Give the position of every leukocyte visible.
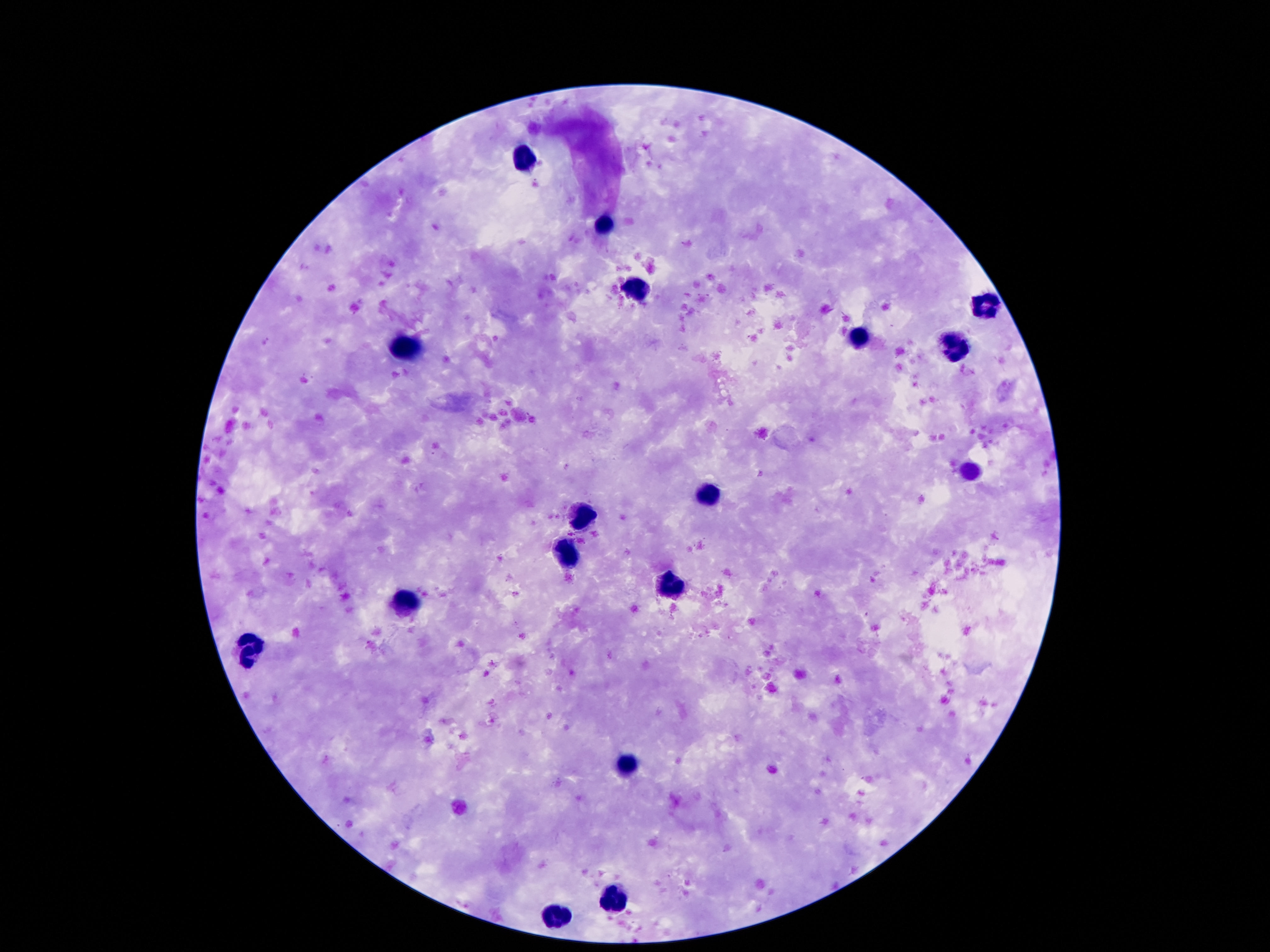
Approximate centers as {x, y} in pixels.
Leukocytes: {528, 160}, {604, 225}, {635, 286}, {984, 307}, {860, 339}, {954, 346}, {408, 347}, {711, 492}, {585, 517}, {568, 555}, {675, 584}, {406, 603}, {251, 649}, {627, 764}, {618, 894}, {557, 919}.

Summary:
  - Image size: 1270×952 pixels
  - Stain: Giemsa
  - Field of view: single
  - Patient malaria status: negative
  - Preparation: thick blood film
  - Magnification: 100x
  - Capture: smartphone camera through the microscope eyepiece